Assess this cell for malaria.
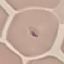

Parasitized.

{
  "capture": "smartphone camera at the microscope eyepiece",
  "preparation": "thin smear",
  "image_type": "automatically extracted cell patch, resized to 64 × 64 pixels",
  "stain": "Giemsa"
}